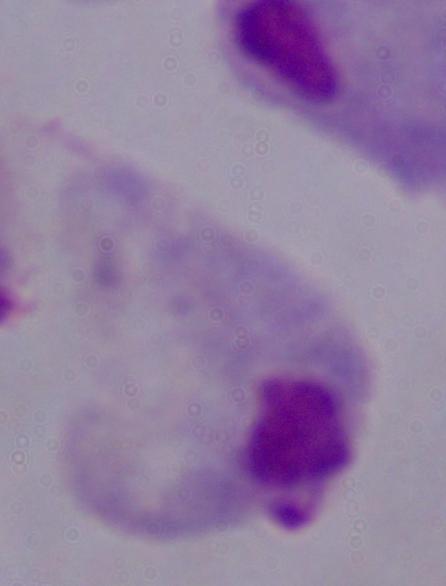
Summary:
  - Identification: trichomonad
  - Magnification: 1000x
  - Modality: photomicrograph